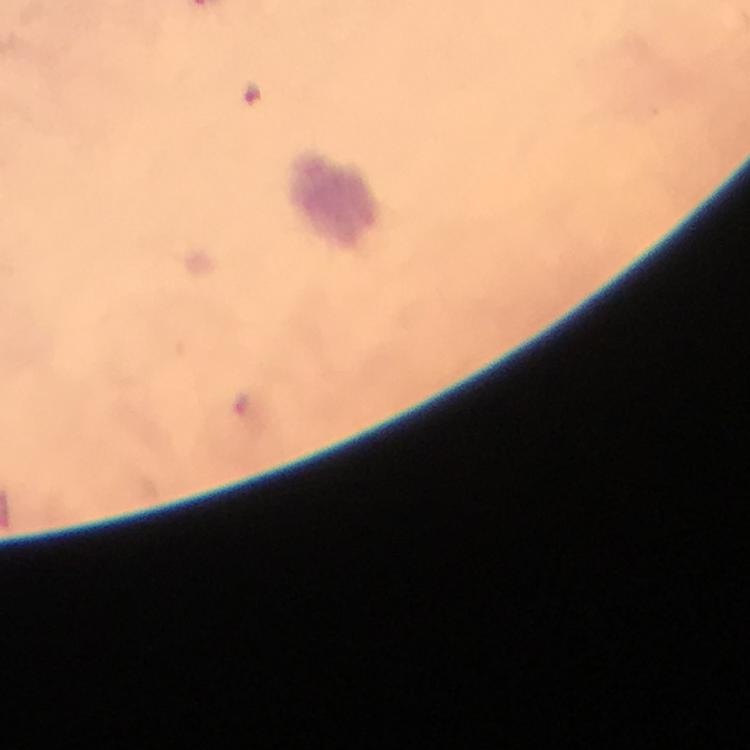
Approximate centers as {x, y} in pixels.
Summary:
  - Plasmodium parasite locations: {254, 95}, {241, 402}
  - Capture: smartphone mounted on the microscope
  - Stain: Giemsa
  - Image size: 750×750 pixels
  - Cropped from: a single field of view
  - Magnification: 100x
  - Preparation: thick blood smear
  - Immersion oil: applied
  - Context: from a malaria diagnostic workup